Name the blood parasite species.
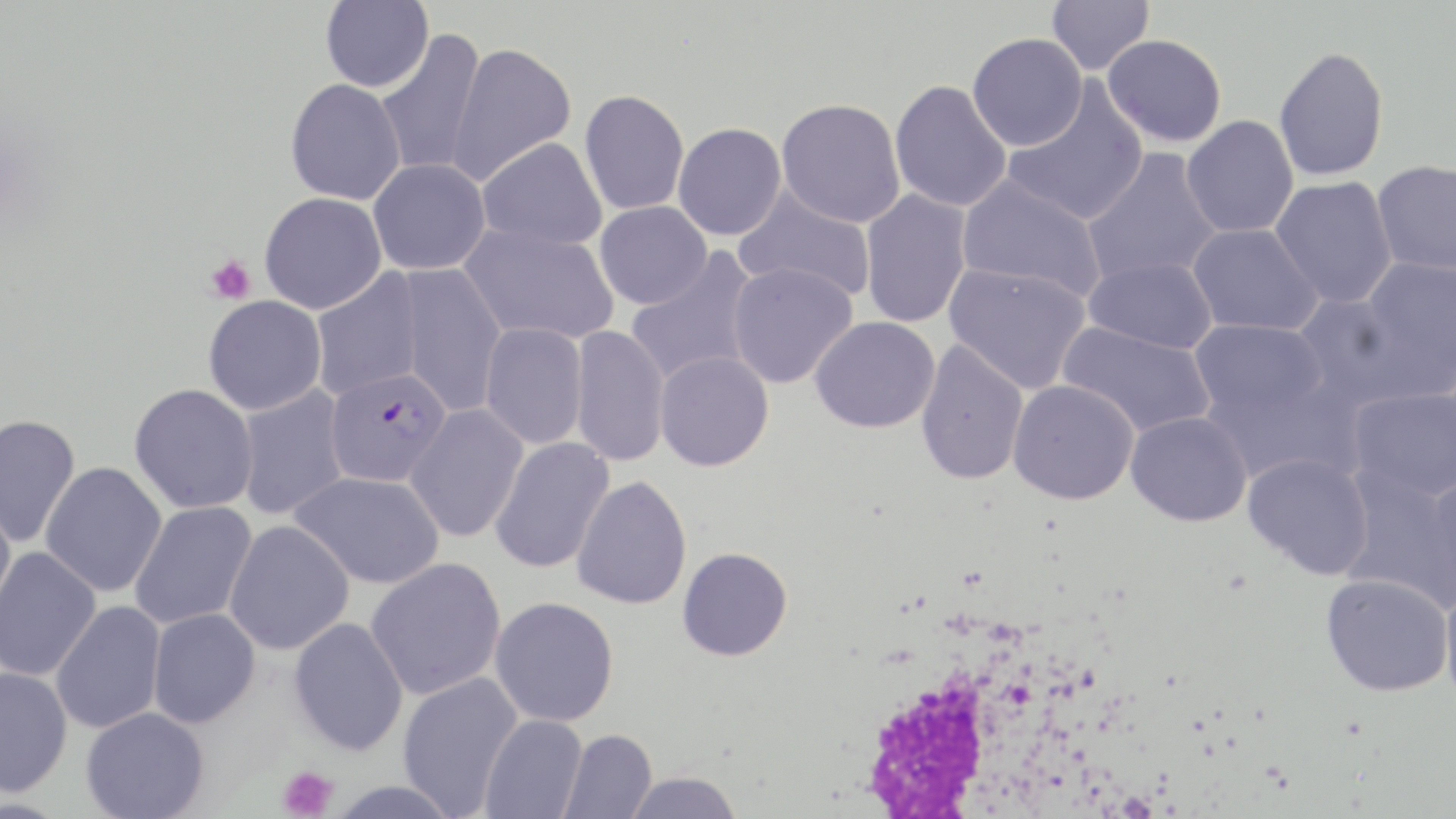
Plasmodium falciparum.

Approximate bounding boxes as (x1,y1)-(x2,y2) corner pairs in pixels. Uninfected red blood cell locations: (320,0)-(433,92), (1046,0)-(1154,76), (373,30)-(487,177), (966,33)-(1087,151), (1102,34)-(1227,147), (445,42)-(576,186), (1273,45)-(1389,180), (284,78)-(406,205), (890,80)-(1012,212), (1003,82)-(1149,226), (579,89)-(689,215), (776,98)-(906,228), (1181,115)-(1299,238), (673,122)-(786,240), (476,137)-(607,251), (1082,148)-(1223,287), (368,158)-(491,276), (1371,160)-(1456,276), (956,175)-(1107,303), (1269,176)-(1397,308), (733,187)-(877,303), (859,189)-(973,329), (259,192)-(386,314), (594,201)-(712,309), (1187,223)-(1323,336), (460,224)-(619,344), (626,248)-(763,388), (1359,256)-(1456,392), (1082,257)-(1217,353), (727,262)-(858,388), (944,263)-(1092,395), (396,264)-(507,417), (310,268)-(425,400), (1290,292)-(1424,409), (203,295)-(327,415), (810,316)-(940,433), (1189,319)-(1328,423), (1057,321)-(1217,439), (479,322)-(588,450), (570,324)-(670,468), (914,340)-(1030,486), (654,350)-(774,471), (1008,380)-(1139,504), (129,383)-(258,513), (235,385)-(350,521), (1347,386)-(1456,502), (405,403)-(529,543), (1126,411)-(1252,526), (0,413)-(81,547), (489,437)-(615,573), (1242,451)-(1374,579), (39,461)-(167,597), (289,470)-(444,589), (1339,471)-(1455,611), (1422,472)-(1456,606), (571,476)-(693,610), (0,498)-(16,621), (129,501)-(257,630), (223,520)-(354,655), (677,547)-(793,661), (0,548)-(101,682), (365,557)-(507,700), (1321,573)-(1453,696), (1439,582)-(1456,711), (489,597)-(619,726), (51,601)-(166,734), (147,608)-(260,728), (288,617)-(409,756), (0,667)-(73,798), (397,671)-(523,816), (81,706)-(209,819), (479,714)-(587,819), (559,729)-(657,819), (622,771)-(743,819), (324,779)-(466,818). Plasmodium falciparum-infected red blood cell locations: (324,366)-(451,486). White blood cell locations: (850,612)-(1086,814). Platelet locations: (205,254)-(255,305), (277,766)-(338,819). One field of a larger specimen. Captured at 1000x magnification. Optical microscopy. Thin blood smear. Image is 1456×819 pixels. May-Grünwald-Giemsa-stained preparation.